Find each parasitized red blood cell.
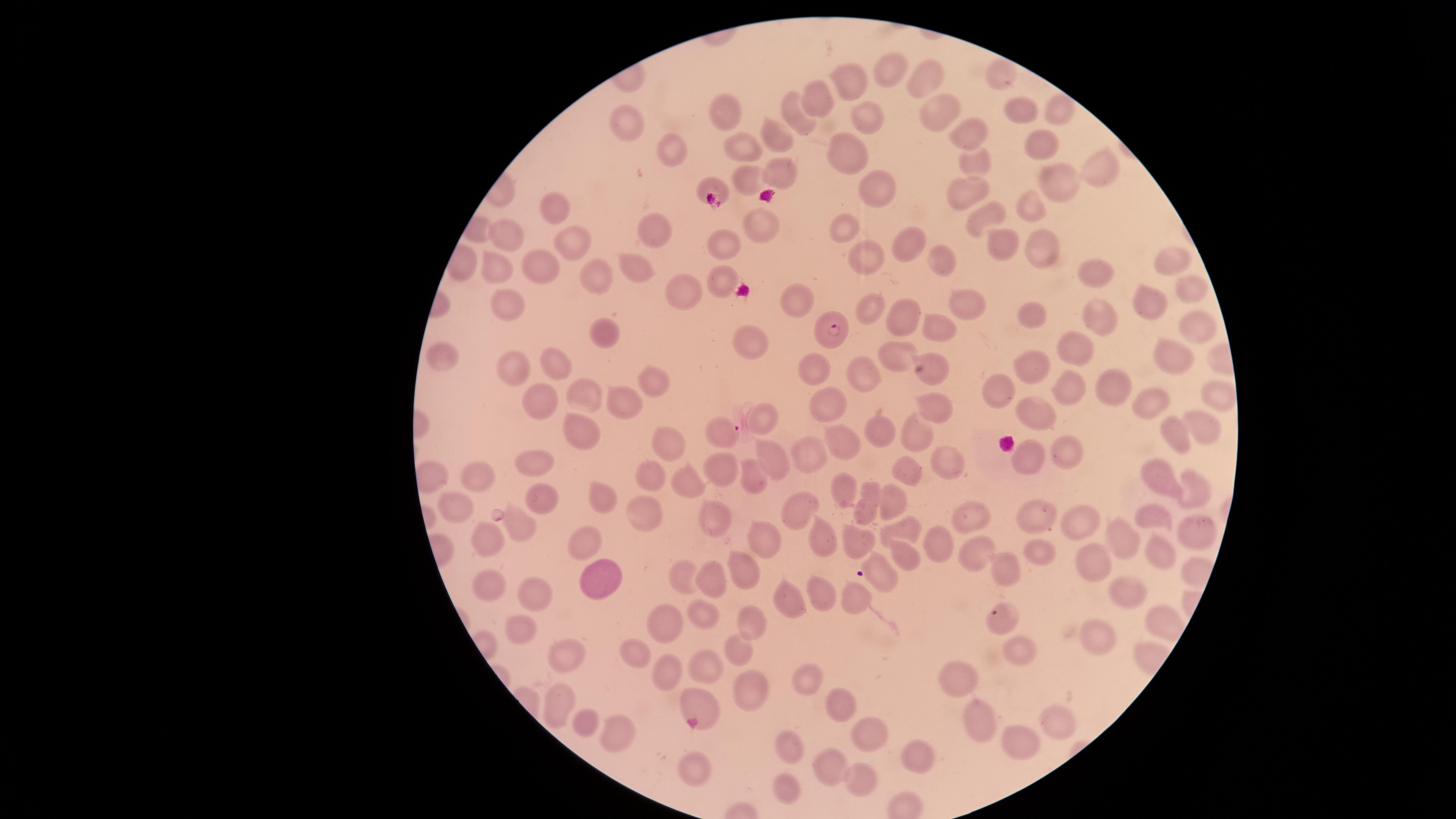

Approximate marker points as [x, y] in pixels.
Parasitized red blood cells: [832, 328], [718, 429].

{
  "preparation": "thin blood film",
  "capture": "smartphone photograph through the microscope eyepiece",
  "stain": "Giemsa",
  "species": "Plasmodium falciparum",
  "uninfected_red_blood_cells": "approximate marker points as [x, y] in pixels: [888, 70], [998, 72], [927, 73], [852, 76], [822, 101], [726, 106], [1018, 107], [934, 109], [794, 112], [1059, 113], [869, 122], [630, 125], [963, 134], [772, 136], [745, 144], [1040, 145], [844, 147], [679, 148], [971, 160], [1096, 166], [747, 175], [782, 176], [1050, 177], [711, 181], [884, 184], [971, 195], [551, 208], [1030, 210], [982, 217], [655, 227], [758, 227], [844, 228], [997, 231], [504, 232], [726, 242], [1042, 242], [572, 244], [900, 246], [861, 253], [938, 258], [534, 261], [1167, 262], [630, 264], [497, 266], [597, 272], [1093, 277], [722, 278], [1187, 285], [684, 295], [796, 295], [1150, 302], [511, 304], [871, 305], [959, 306], [900, 309], [1090, 310], [1032, 313], [1197, 328], [933, 330], [601, 333], [1071, 346], [743, 347], [442, 353], [893, 356], [553, 359], [1169, 359], [929, 364], [1029, 364], [819, 369], [514, 374], [656, 380], [863, 380], [1102, 383], [1068, 390], [998, 394], [624, 395], [584, 396], [1146, 396], [1212, 396], [829, 402], [539, 403], [930, 409], [1032, 413], [761, 415], [1201, 426], [909, 429], [584, 431], [1175, 435], [879, 436], [672, 442], [849, 444], [811, 449], [1068, 451], [1029, 454], [532, 460], [775, 460], [942, 462], [721, 464], [481, 471], [751, 472], [907, 473], [653, 474], [1162, 474], [684, 478], [1190, 486], [844, 490], [604, 494], [548, 496], [899, 503], [458, 504], [641, 508], [867, 508], [805, 509], [712, 512], [1038, 512], [969, 516], [1077, 518], [1156, 520], [512, 524], [1191, 528], [901, 530], [1114, 534], [821, 536], [860, 540], [493, 541], [583, 541], [766, 542], [944, 549], [901, 554], [970, 554], [1165, 554], [1035, 555], [1095, 562], [741, 565], [1004, 565], [607, 577], [486, 578], [678, 578], [886, 578], [714, 580], [817, 589], [527, 591], [782, 595], [1117, 597], [854, 598], [696, 613], [664, 619], [747, 620], [996, 620], [1153, 620], [518, 624], [1094, 640], [739, 648], [636, 650], [1017, 650], [565, 657], [709, 667], [665, 668], [957, 676], [799, 679], [746, 689], [559, 700], [835, 700], [694, 703], [980, 719], [1053, 720], [587, 723], [613, 733], [862, 733], [1023, 736], [784, 750], [914, 759], [831, 768], [690, 769], [866, 781], [786, 782]",
  "image_size": "1456×819 pixels",
  "field_of_view": "single",
  "visible_region": "circular"
}